Comment on the morphology of the red blood cells.
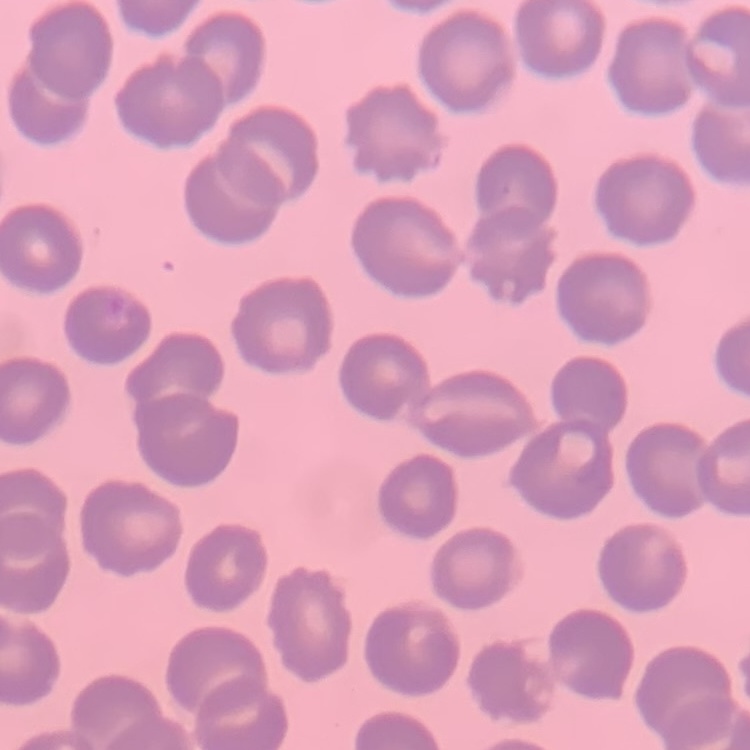
No rouleaux formation.

{
  "preparation": "thin blood film",
  "image_type": "one tile cut from a larger photomicrograph",
  "stain": "Field's or Giemsa"
}